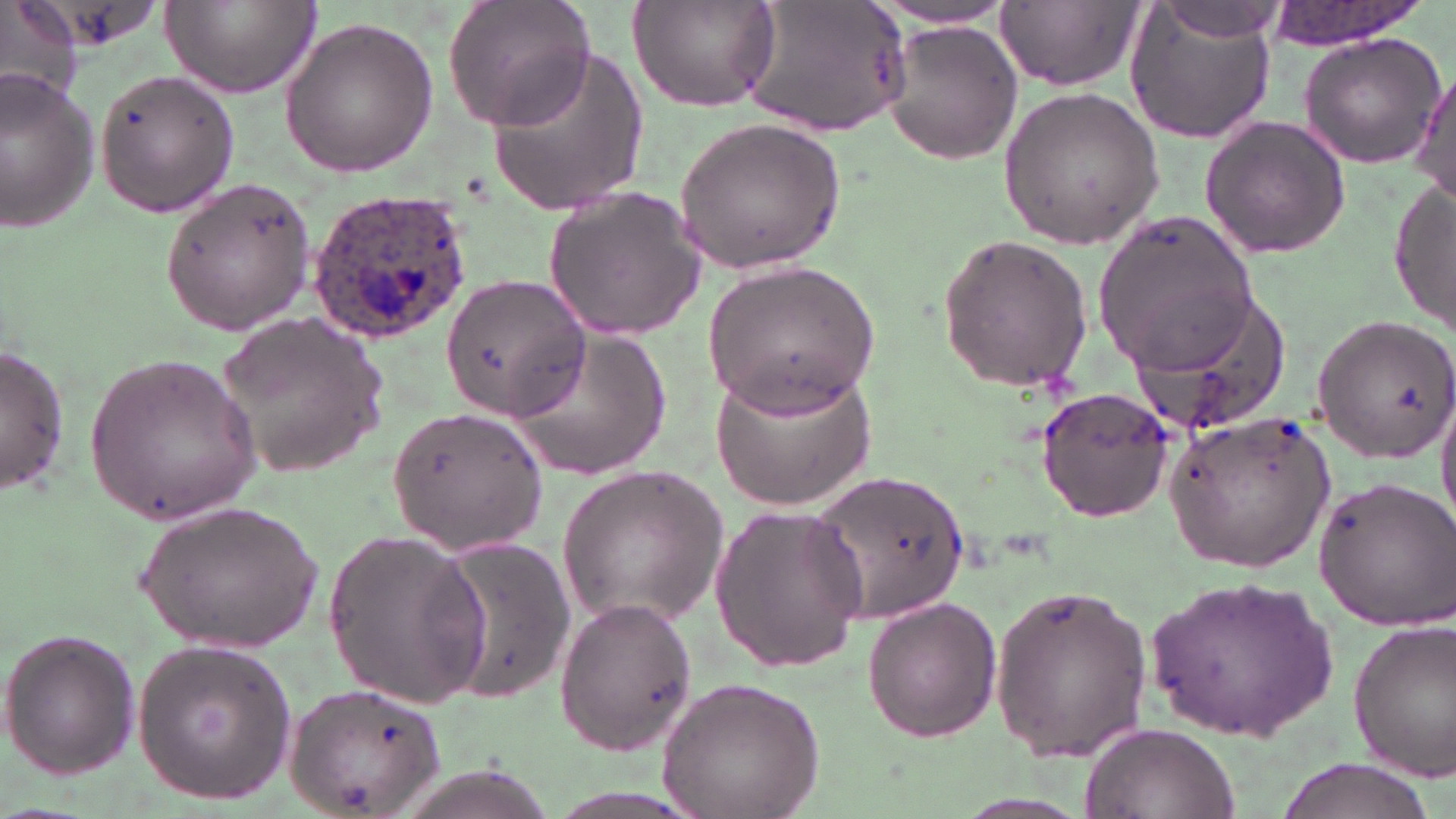

{
  "slide_level_diagnosis": "Plasmodium ovale",
  "uninfected_red_blood_cell_locations": "approximate bounding boxes as (x1,y1)-(x2,y2) corner pairs in pixels: (1,0)-(85,109), (163,0)-(319,99), (445,0)-(596,131), (743,1)-(911,137), (995,1)-(1140,89), (1259,1)-(1437,49), (628,2)-(781,112), (865,4)-(1024,30), (1155,4)-(1286,44), (1122,9)-(1281,147), (278,16)-(440,179), (883,20)-(1021,164), (1296,31)-(1446,170), (482,44)-(648,213), (1408,64)-(1454,205), (96,67)-(239,219), (0,69)-(103,232), (998,86)-(1165,248), (1199,114)-(1353,259), (673,116)-(848,277), (161,178)-(318,335), (1389,180)-(1456,336), (542,185)-(709,340), (1095,211)-(1258,369), (934,231)-(1096,393), (701,258)-(883,415), (440,275)-(590,422), (1120,287)-(1295,441), (215,310)-(390,480), (1309,312)-(1456,461), (511,325)-(673,475), (1,343)-(71,497), (84,350)-(267,523), (709,358)-(880,512), (1034,386)-(1177,521), (1435,388)-(1456,531), (384,403)-(548,557), (1166,409)-(1337,570), (556,463)-(730,628), (809,471)-(969,624), (1312,475)-(1456,629), (134,498)-(326,654), (708,501)-(868,674), (324,529)-(491,706), (426,538)-(573,703), (1148,571)-(1339,741), (987,580)-(1152,765), (553,595)-(697,755), (862,598)-(1003,743), (1347,617)-(1456,780), (1,627)-(140,780), (131,639)-(296,807), (658,677)-(824,818), (284,678)-(449,819), (1083,723)-(1239,819), (1276,757)-(1441,819)",
  "field_of_view": "single",
  "stain": "May-Grünwald-Giemsa",
  "magnification": "1000x",
  "plasmodium_ovale_infected_red_blood_cell_locations": "approximate bounding boxes as (x1,y1)-(x2,y2) corner pairs in pixels: (305,189)-(474,344)",
  "preparation": "thin blood smear",
  "image_size": "1456×819 pixels",
  "modality": "light microscopy"
}